Assess this cell for malaria.
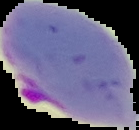
It is parasitized.

Image is 139×130 pixels. From a thin blood film. Cell region segmented out of the field of view; the surrounding area is masked to black.